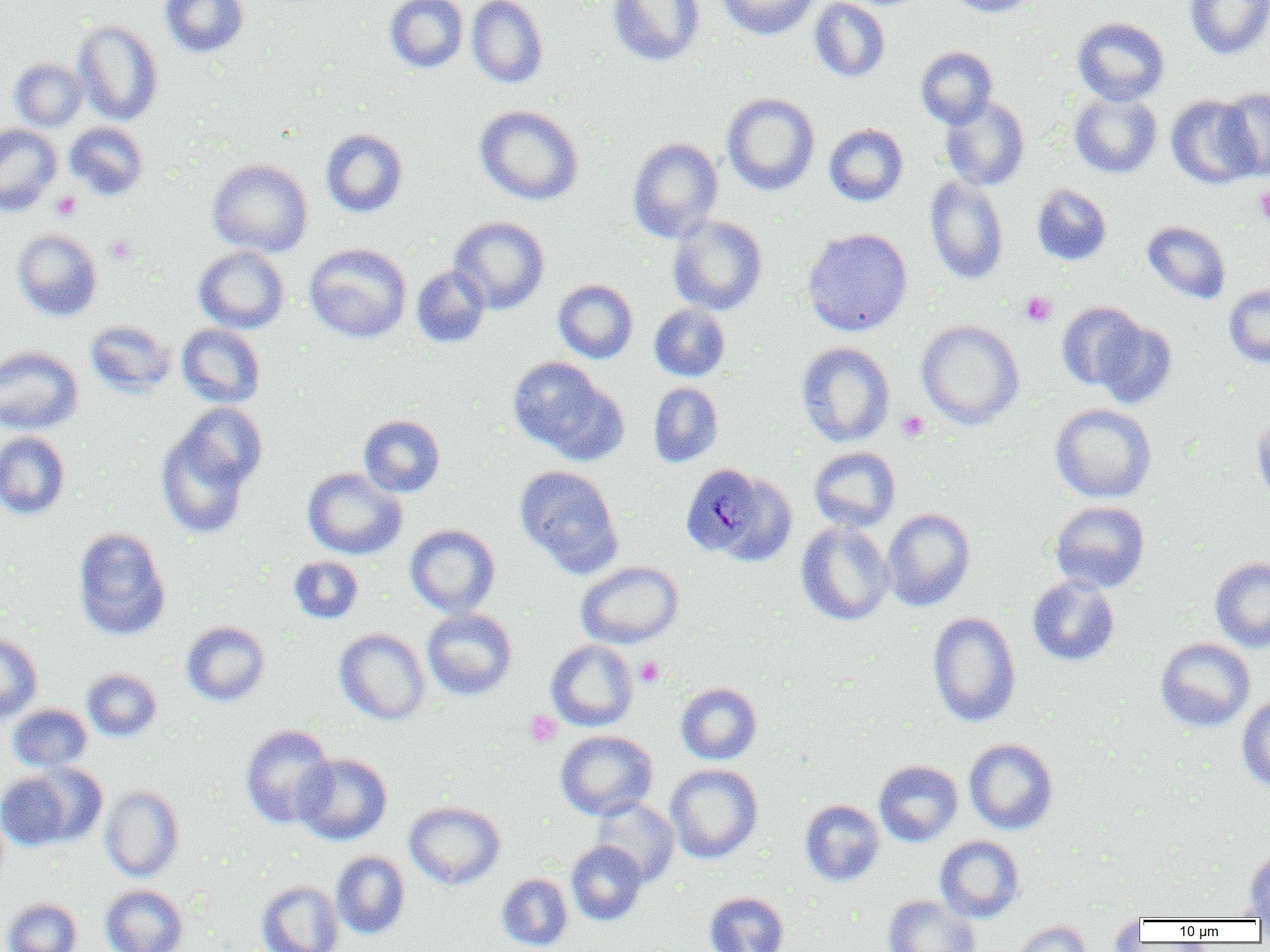
Summary:
  - Coordinate format: approximate bounding boxes as named x1/y1/x2/y2 corners in pixels
  - Plasmodium malariae-infected red blood cell locations: (x1=678, y1=462, x2=765, y2=562)
  - Platelet locations: (x1=1255, y1=186, x2=1270, y2=226), (x1=50, y1=190, x2=81, y2=221), (x1=104, y1=236, x2=136, y2=265), (x1=1020, y1=291, x2=1056, y2=327), (x1=896, y1=411, x2=929, y2=441), (x1=635, y1=657, x2=664, y2=687), (x1=524, y1=710, x2=561, y2=747)
  - Uninfected red blood cell locations: (x1=159, y1=0, x2=249, y2=58), (x1=384, y1=0, x2=468, y2=73), (x1=466, y1=0, x2=548, y2=89), (x1=607, y1=0, x2=704, y2=66), (x1=715, y1=0, x2=820, y2=40), (x1=809, y1=0, x2=890, y2=83), (x1=943, y1=0, x2=1042, y2=18), (x1=1184, y1=0, x2=1270, y2=59), (x1=1072, y1=17, x2=1170, y2=106), (x1=73, y1=20, x2=164, y2=126), (x1=915, y1=46, x2=998, y2=128), (x1=9, y1=57, x2=88, y2=131), (x1=1216, y1=86, x2=1270, y2=180), (x1=1069, y1=91, x2=1162, y2=179), (x1=721, y1=92, x2=820, y2=196), (x1=1166, y1=95, x2=1260, y2=189), (x1=940, y1=96, x2=1030, y2=191), (x1=474, y1=104, x2=584, y2=206), (x1=64, y1=121, x2=149, y2=201), (x1=0, y1=123, x2=62, y2=217), (x1=824, y1=124, x2=908, y2=206), (x1=320, y1=129, x2=408, y2=217), (x1=627, y1=137, x2=724, y2=243), (x1=207, y1=159, x2=313, y2=257), (x1=924, y1=175, x2=1009, y2=284), (x1=1031, y1=184, x2=1112, y2=266), (x1=667, y1=215, x2=767, y2=315), (x1=449, y1=216, x2=550, y2=315), (x1=1141, y1=220, x2=1231, y2=305), (x1=802, y1=228, x2=913, y2=336), (x1=11, y1=229, x2=103, y2=322), (x1=304, y1=243, x2=412, y2=343), (x1=193, y1=245, x2=289, y2=334), (x1=411, y1=265, x2=490, y2=348), (x1=553, y1=279, x2=638, y2=364), (x1=1223, y1=284, x2=1270, y2=368), (x1=1056, y1=302, x2=1146, y2=391), (x1=649, y1=303, x2=731, y2=381), (x1=1092, y1=318, x2=1177, y2=409), (x1=84, y1=320, x2=176, y2=398), (x1=916, y1=320, x2=1025, y2=429), (x1=176, y1=324, x2=266, y2=408), (x1=796, y1=342, x2=895, y2=448), (x1=0, y1=345, x2=84, y2=435), (x1=507, y1=357, x2=620, y2=459), (x1=648, y1=382, x2=723, y2=467), (x1=173, y1=402, x2=267, y2=493), (x1=1050, y1=403, x2=1157, y2=503), (x1=1250, y1=412, x2=1270, y2=508), (x1=358, y1=415, x2=445, y2=497), (x1=156, y1=422, x2=254, y2=539), (x1=0, y1=431, x2=70, y2=519), (x1=809, y1=446, x2=900, y2=532), (x1=514, y1=465, x2=623, y2=576), (x1=302, y1=467, x2=407, y2=559), (x1=1049, y1=500, x2=1150, y2=593), (x1=881, y1=507, x2=975, y2=611), (x1=795, y1=521, x2=894, y2=626), (x1=404, y1=524, x2=501, y2=617), (x1=72, y1=527, x2=171, y2=641), (x1=288, y1=556, x2=363, y2=624), (x1=1210, y1=557, x2=1270, y2=654), (x1=575, y1=561, x2=683, y2=648), (x1=1027, y1=576, x2=1119, y2=666), (x1=422, y1=609, x2=518, y2=700), (x1=927, y1=611, x2=1021, y2=727), (x1=181, y1=621, x2=270, y2=706), (x1=334, y1=628, x2=430, y2=725), (x1=0, y1=632, x2=43, y2=724), (x1=1155, y1=638, x2=1255, y2=732), (x1=546, y1=640, x2=638, y2=732), (x1=81, y1=668, x2=162, y2=741), (x1=675, y1=682, x2=762, y2=764), (x1=1236, y1=695, x2=1270, y2=792), (x1=7, y1=704, x2=92, y2=772), (x1=240, y1=724, x2=337, y2=828), (x1=555, y1=730, x2=658, y2=820), (x1=963, y1=738, x2=1058, y2=835), (x1=293, y1=753, x2=392, y2=845), (x1=874, y1=760, x2=963, y2=846), (x1=665, y1=764, x2=763, y2=863), (x1=0, y1=769, x2=82, y2=850), (x1=100, y1=785, x2=184, y2=881), (x1=589, y1=798, x2=679, y2=887), (x1=800, y1=799, x2=885, y2=886), (x1=404, y1=800, x2=506, y2=890), (x1=934, y1=835, x2=1025, y2=923), (x1=566, y1=840, x2=647, y2=926), (x1=1243, y1=849, x2=1270, y2=919), (x1=331, y1=850, x2=410, y2=939), (x1=496, y1=873, x2=573, y2=951), (x1=256, y1=880, x2=344, y2=952), (x1=99, y1=884, x2=189, y2=952), (x1=704, y1=891, x2=789, y2=952), (x1=883, y1=895, x2=979, y2=952), (x1=2, y1=898, x2=82, y2=952), (x1=1108, y1=912, x2=1144, y2=951), (x1=1008, y1=920, x2=1092, y2=952)
  - Slide-level diagnosis: Plasmodium malariae
  - Preparation: thin blood film
  - Magnification: 1000x
  - Field of view: one of a larger specimen
  - Modality: light microscopy
  - Image size: 1270×952 pixels